Report the malaria status of this cell.
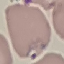

Parasitized.

preparation = thin blood smear
capture = smartphone through the microscope eyepiece
image type = automatically extracted cell patch, resized to 64 × 64 pixels
stain = Giemsa